Classify this cell by malaria status.
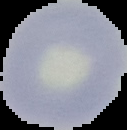
Uninfected.

From a thin blood smear. Image is 127×130 pixels. The area outside the segmented cell region is set to black.